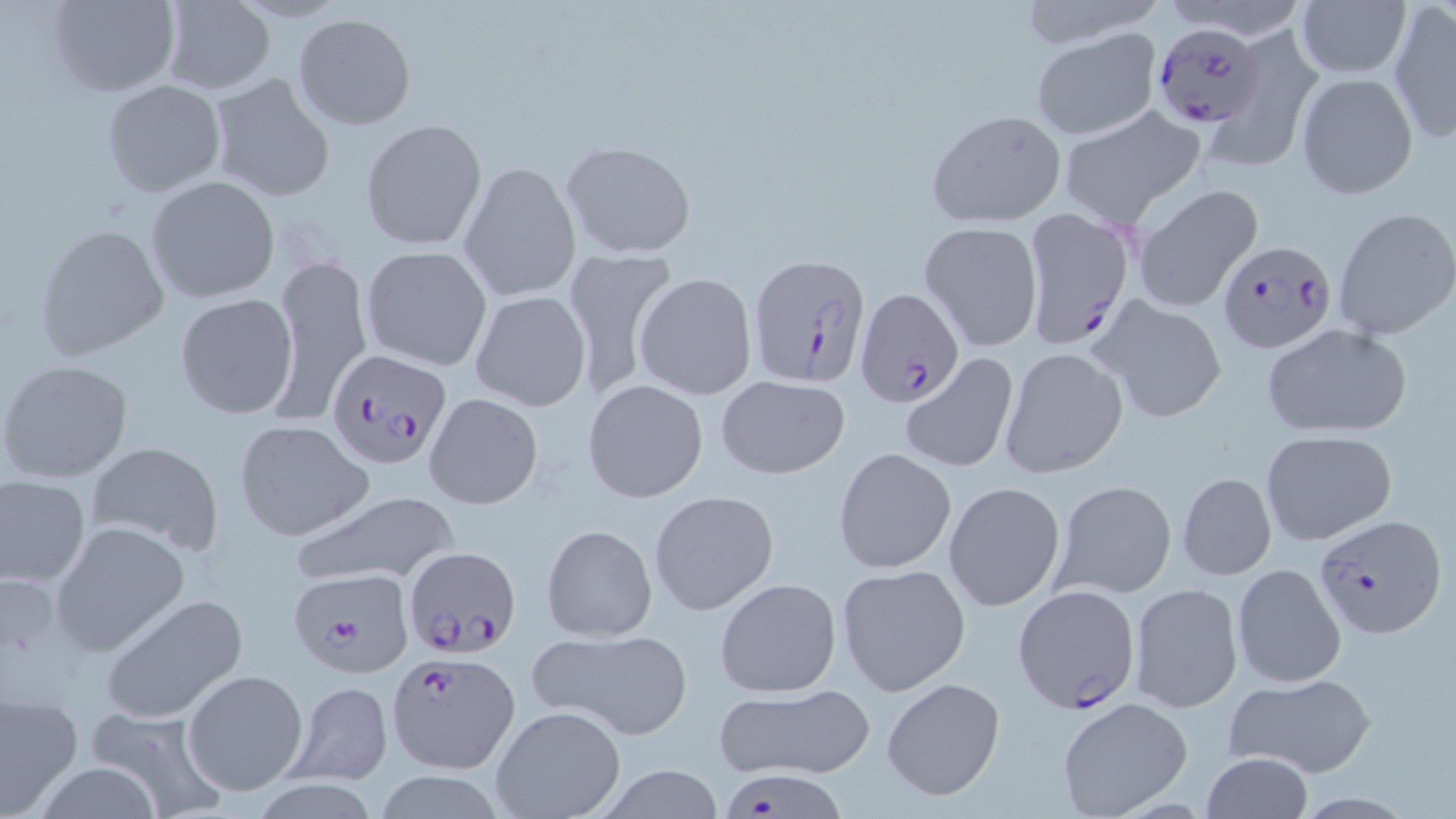

{
  "slide_level_diagnosis": "Plasmodium falciparum",
  "field_of_view": "single",
  "preparation": "thin blood film",
  "image_size": "1456×819 pixels",
  "magnification": "1000x",
  "uninfected_red_blood_cell_locations": "approximate bounding boxes as (x1,y1)-(x2,y2) corner pairs in pixels: (1013,0)-(1163,50), (1296,0)-(1408,80), (158,1)-(276,94), (44,2)-(180,97), (1388,4)-(1456,143), (292,12)-(418,130), (1032,29)-(1160,140), (1209,29)-(1325,177), (1296,72)-(1418,198), (208,73)-(336,202), (102,80)-(226,197), (1059,104)-(1206,227), (925,108)-(1066,227), (360,119)-(487,249), (557,139)-(698,259), (457,160)-(581,302), (145,175)-(280,303), (1131,185)-(1262,311), (1333,206)-(1456,339), (920,221)-(1043,351), (33,224)-(169,359), (360,245)-(493,371), (267,249)-(372,424), (561,249)-(679,404), (634,272)-(758,400), (469,289)-(592,412), (175,294)-(299,419), (1092,298)-(1228,424), (1260,323)-(1412,439), (998,348)-(1127,477), (897,352)-(1019,473), (0,359)-(133,483), (716,374)-(849,478), (582,379)-(707,501), (424,392)-(545,510), (232,419)-(372,541), (1260,429)-(1397,545), (84,440)-(223,557), (833,447)-(957,574), (0,473)-(90,589), (1175,473)-(1275,582), (1051,480)-(1177,600), (944,482)-(1066,613), (288,489)-(462,587), (649,490)-(780,615), (50,521)-(190,656), (540,524)-(657,643), (835,563)-(972,697), (1231,564)-(1346,687), (715,576)-(842,698), (1128,583)-(1243,711), (99,593)-(248,724), (527,628)-(693,740), (181,669)-(310,796), (1224,673)-(1377,778), (881,677)-(1005,802), (283,681)-(395,786), (711,683)-(875,780), (0,689)-(85,818), (1056,697)-(1193,818), (83,705)-(228,818), (489,706)-(625,819), (1200,752)-(1313,819), (591,764)-(731,819), (371,768)-(510,819)",
  "modality": "optical microscopy",
  "stain": "May-Grünwald-Giemsa",
  "plasmodium_falciparum_infected_red_blood_cell_locations": "approximate bounding boxes as (x1,y1)-(x2,y2) corner pairs in pixels: (1154,22)-(1265,128), (1021,207)-(1138,352), (1216,239)-(1336,353), (748,252)-(870,386), (855,289)-(963,409), (322,347)-(450,468), (1314,513)-(1446,640), (401,544)-(521,656), (287,569)-(416,679), (1012,584)-(1141,713), (385,650)-(519,775)"
}